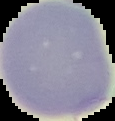

Summary:
  - Image type: segmented cell region on a black background
  - Malaria status: uninfected
  - Image size: 115×121 pixels
  - Preparation: thin blood film